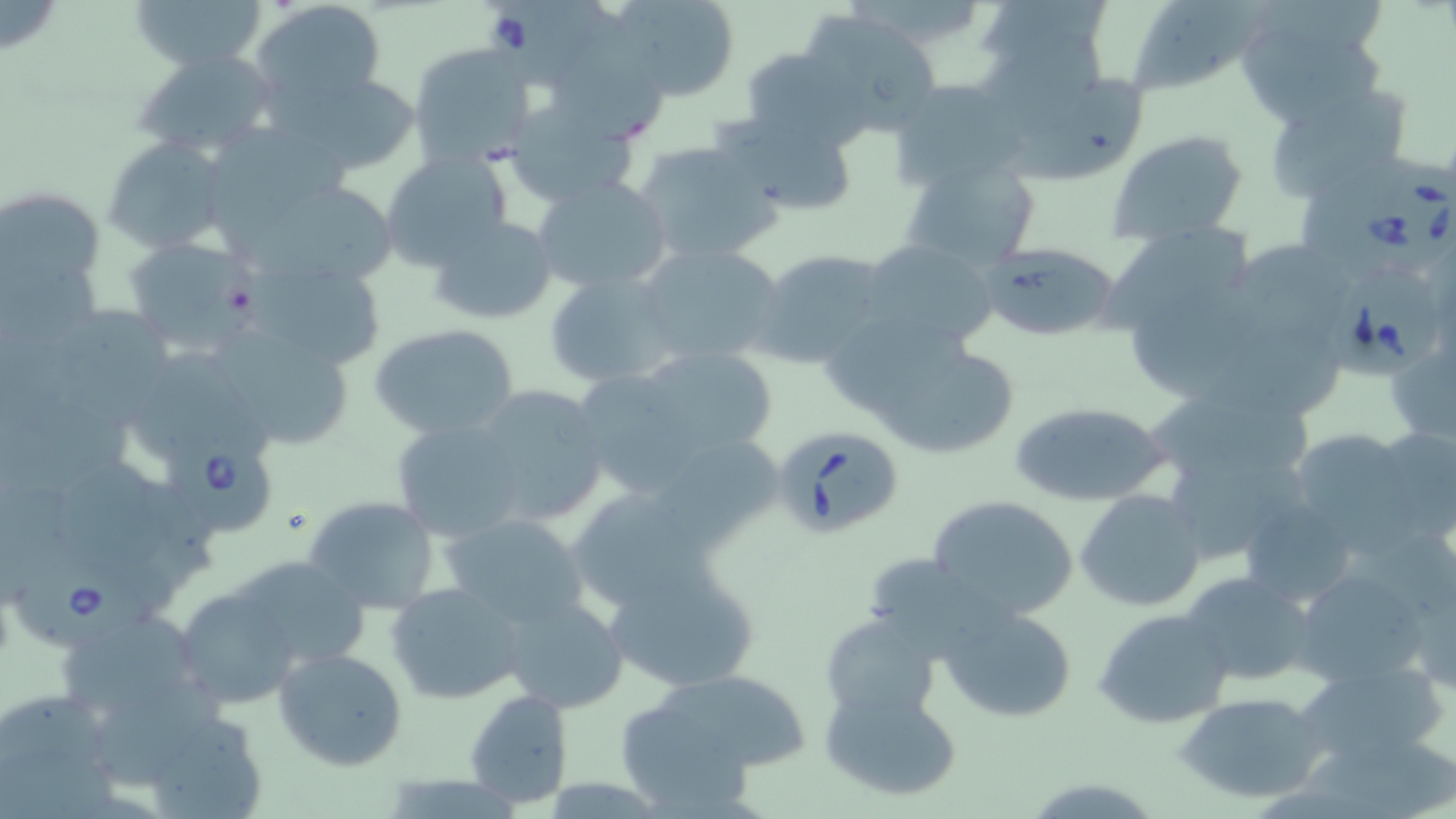

Approximate bounding boxes as (x1,y1)-(x2,y2) corner pairs in pixels. Babesia divergens-infected red blood cell locations: (492,0)-(621,95), (1331,163)-(1456,282), (1322,265)-(1441,379), (771,424)-(906,540), (165,435)-(273,533), (13,558)-(161,653). Uninfected red blood cell locations: (130,0)-(268,75), (251,0)-(386,111), (609,0)-(739,101), (1127,1)-(1270,96), (1231,3)-(1392,126), (796,9)-(946,136), (555,12)-(677,146), (975,37)-(1114,143), (409,42)-(538,170), (738,46)-(872,151), (134,50)-(275,161), (276,71)-(423,176), (1013,74)-(1152,189), (885,77)-(1029,190), (1260,82)-(1412,203), (506,99)-(641,209), (722,110)-(862,220), (1105,129)-(1251,245), (104,137)-(231,254), (635,140)-(781,267), (379,152)-(514,272), (896,157)-(1040,273), (531,175)-(673,298), (238,177)-(404,287), (1,186)-(108,312), (428,215)-(561,326), (1097,221)-(1261,337), (122,236)-(256,356), (859,239)-(1000,351), (638,242)-(788,370), (1228,242)-(1364,342), (979,243)-(1121,341), (753,248)-(894,369), (0,253)-(108,347), (242,255)-(387,372), (542,270)-(680,388), (1128,290)-(1261,407), (52,309)-(186,428), (368,323)-(521,439), (1224,324)-(1338,421), (837,325)-(1021,462), (215,333)-(355,451), (1385,337)-(1455,447), (635,347)-(780,460), (128,348)-(283,469), (576,373)-(704,492), (468,383)-(609,526), (1143,383)-(1331,493), (1008,402)-(1174,508), (387,413)-(530,545), (1369,425)-(1456,545), (1286,428)-(1424,547), (646,430)-(790,553), (63,456)-(173,581), (565,484)-(709,610), (1075,490)-(1206,612), (927,493)-(1079,621), (302,495)-(443,614), (1238,496)-(1362,608), (1211,505)-(1343,675), (439,509)-(589,629), (597,556)-(764,694), (223,558)-(374,667), (1291,563)-(1437,691), (1177,572)-(1319,687), (386,581)-(525,705), (178,590)-(298,707), (501,595)-(628,713), (938,605)-(1080,724), (47,606)-(204,720), (1095,608)-(1234,729), (820,613)-(945,726), (272,647)-(408,769), (1296,662)-(1446,767), (632,667)-(807,785), (98,684)-(231,788), (820,686)-(962,802), (464,688)-(575,809), (1177,691)-(1331,804), (1307,747)-(1456,818). Slide-level diagnosis: Babesia divergens. May-Grünwald-Giemsa stain. Captured at 1000x magnification. Image is 1456×819 pixels. Light microscopy. Single field of view. Thin blood film.